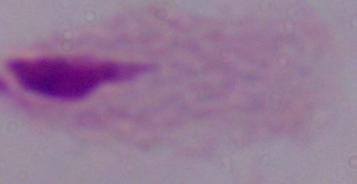
A trichomonad is shown. Micrograph. Captured at 1000x magnification.